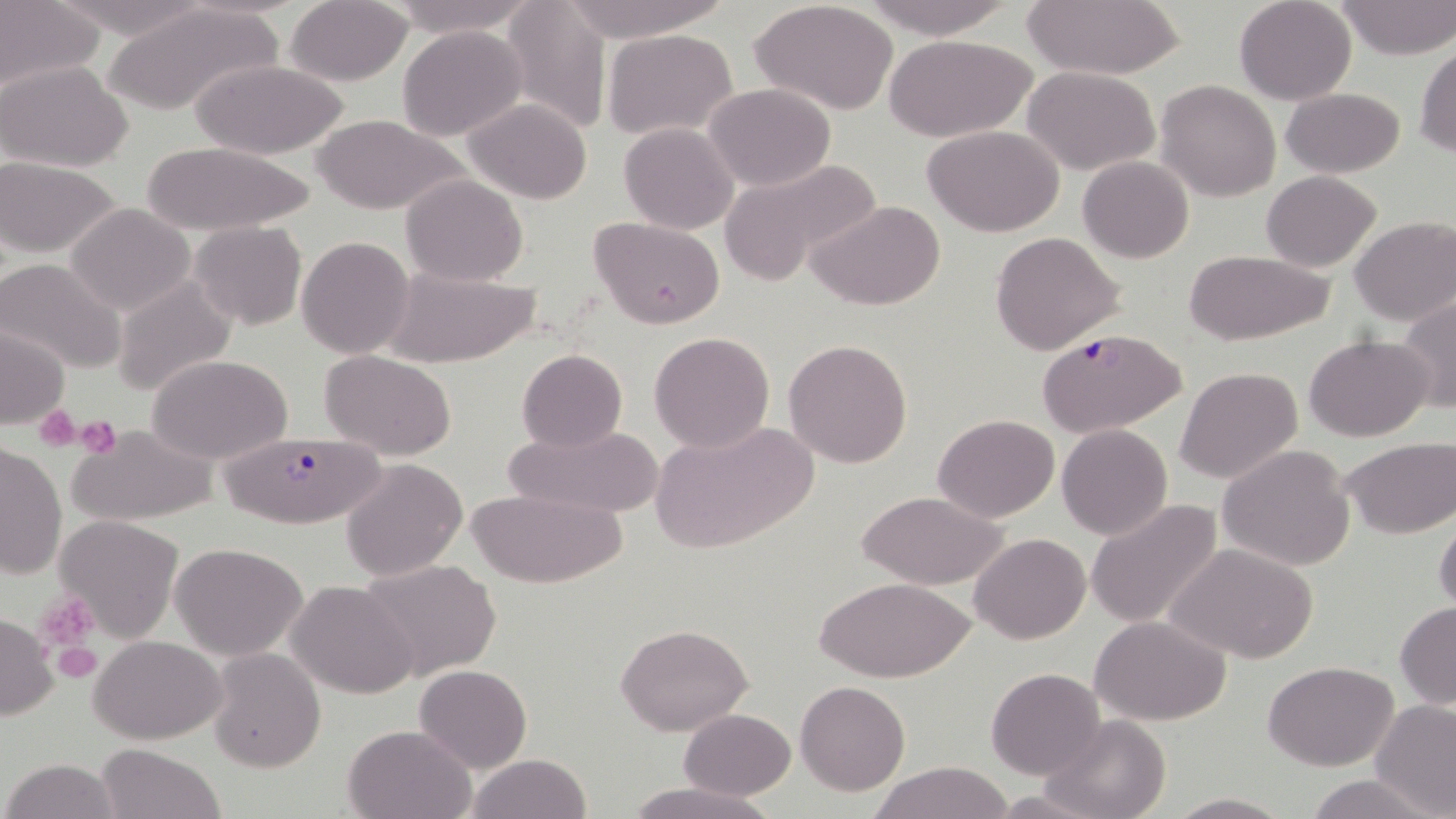
Summary:
  - Coordinate format: approximate bounding boxes as [x1, y1, x2, y2] in pixels
  - Uninfected red blood cell locations: [382, 0, 533, 36], [499, 0, 612, 131], [557, 0, 727, 43], [862, 0, 1013, 37], [1021, 0, 1187, 79], [1234, 0, 1356, 104], [1334, 0, 1456, 59], [0, 1, 103, 93], [102, 2, 282, 116], [285, 2, 412, 86], [752, 3, 899, 115], [398, 26, 527, 141], [603, 29, 739, 141], [886, 34, 1037, 143], [1415, 43, 1456, 158], [194, 60, 351, 159], [1, 61, 133, 169], [166, 63, 335, 231], [1021, 65, 1162, 176], [1156, 79, 1280, 202], [703, 83, 836, 191], [1281, 86, 1405, 178], [463, 98, 595, 203], [311, 114, 467, 216], [619, 122, 739, 234], [924, 127, 1064, 237], [134, 139, 322, 236], [718, 155, 881, 282], [1077, 155, 1195, 263], [0, 159, 124, 257], [1261, 171, 1381, 270], [401, 175, 529, 287], [808, 200, 946, 312], [63, 203, 196, 316], [589, 215, 726, 329], [1350, 216, 1456, 325], [190, 220, 306, 330], [991, 231, 1126, 356], [297, 236, 415, 358], [1182, 250, 1337, 344], [0, 258, 126, 376], [382, 267, 539, 366], [113, 274, 237, 399], [1398, 294, 1456, 413], [0, 326, 71, 429], [650, 331, 775, 454], [1303, 334, 1434, 441], [782, 338, 912, 468], [516, 348, 628, 451], [320, 350, 458, 459], [146, 353, 295, 463], [1175, 366, 1303, 483], [933, 413, 1060, 524], [650, 420, 817, 557], [67, 422, 217, 527], [503, 422, 662, 521], [1056, 424, 1172, 540], [1338, 437, 1456, 538], [0, 441, 66, 581], [1217, 444, 1356, 571], [340, 458, 467, 580], [468, 487, 627, 589], [857, 491, 1007, 589], [1085, 499, 1224, 630], [1433, 510, 1456, 616], [54, 515, 185, 641], [969, 533, 1091, 643], [172, 543, 309, 660], [1167, 543, 1319, 663], [357, 557, 502, 680], [813, 575, 975, 681], [286, 580, 419, 699], [1395, 604, 1456, 710], [0, 613, 58, 721], [1089, 615, 1232, 724], [614, 623, 752, 735], [90, 636, 226, 743], [207, 649, 325, 771], [1263, 660, 1400, 771], [414, 664, 532, 774], [988, 668, 1106, 780], [796, 681, 909, 795], [1370, 701, 1456, 818], [680, 708, 796, 799], [1043, 714, 1174, 819], [342, 723, 478, 818], [96, 744, 223, 819], [465, 753, 592, 819], [2, 758, 124, 818], [867, 763, 1016, 819], [1304, 774, 1435, 818], [624, 781, 774, 819], [986, 791, 1104, 818], [1166, 792, 1293, 818]
  - Plasmodium falciparum-infected red blood cell locations: [1037, 328, 1186, 438], [221, 427, 397, 531]
  - Platelet locations: [34, 405, 80, 452], [73, 415, 121, 458], [36, 593, 100, 651], [50, 636, 103, 684]
  - Slide-level diagnosis: Plasmodium falciparum
  - Magnification: 1000x
  - Field of view: one of a larger specimen
  - Preparation: thin blood smear
  - Stain: May-Grünwald-Giemsa
  - Image size: 1456×819 pixels
  - Modality: light microscopy